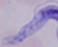
Summary:
  - Modality: micrograph
  - Magnification: 1000x
  - Identification: trypanosome